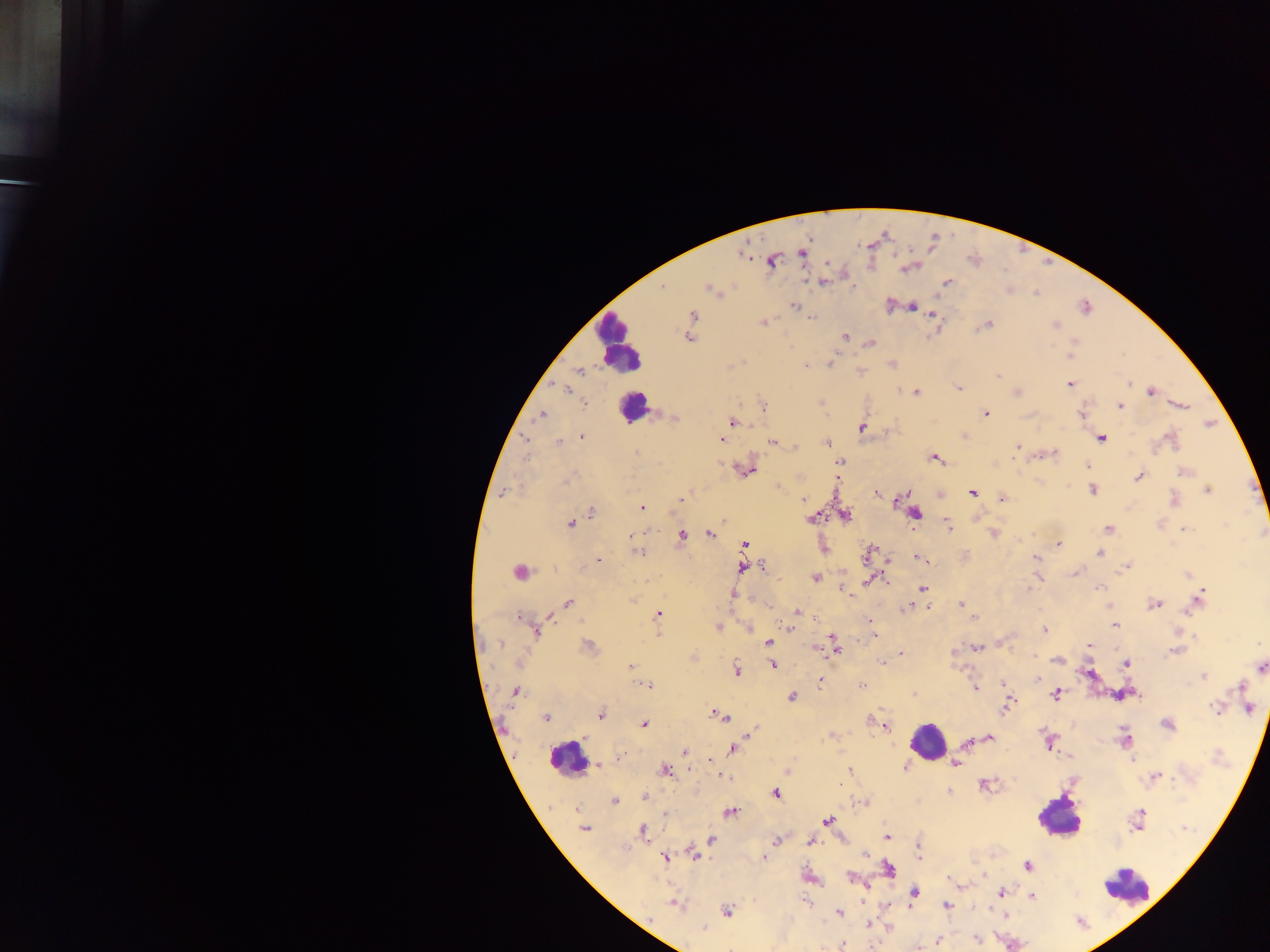

Approximate centers as {x, y} in pixels.
Summary:
  - Leukocyte locations: {618, 343}, {633, 406}, {927, 740}, {567, 758}, {1058, 816}, {1126, 886}
  - Malaria parasite locations: {742, 252}, {802, 253}, {773, 260}, {827, 263}, {907, 267}, {823, 282}, {947, 283}, {662, 286}, {710, 288}, {890, 305}, {794, 306}, {911, 306}, {933, 314}, {691, 316}, {812, 317}, {763, 322}, {987, 324}, {1056, 324}, {845, 336}, {690, 337}, {1073, 340}, {871, 343}, {1070, 355}, {830, 362}, {892, 364}, {805, 366}, {578, 369}, {861, 370}, {997, 375}, {1070, 384}, {566, 388}, {959, 388}, {1016, 391}, {1149, 391}, {914, 392}, {584, 402}, {821, 402}, {1180, 404}, {762, 405}, {1120, 406}, {986, 413}, {540, 414}, {1081, 414}, {672, 416}, {732, 421}, {1209, 423}, {862, 427}, {965, 435}, {582, 437}, {523, 438}, {720, 438}, {1100, 438}, {1171, 440}, {772, 441}, {558, 442}, {825, 443}, {1017, 446}, {795, 447}, {1052, 453}, {636, 454}, {934, 458}, {839, 463}, {1087, 465}, {744, 469}, {1184, 471}, {799, 476}, {1139, 476}, {777, 485}, {1092, 490}, {1207, 490}, {503, 492}, {972, 492}, {877, 493}, {903, 495}, {941, 495}, {1003, 498}, {681, 499}, {803, 499}, {1174, 500}, {642, 507}, {591, 512}, {915, 514}, {844, 515}, {811, 517}, {975, 517}, {724, 520}, {570, 523}, {947, 524}, {1108, 529}, {1184, 529}, {709, 533}, {993, 533}, {629, 535}, {681, 536}, {1057, 543}, {744, 545}, {823, 547}, {638, 552}, {868, 553}, {1099, 553}, {920, 558}, {886, 559}, {1035, 559}, {598, 561}, {762, 566}, {1126, 566}, {743, 567}, {519, 572}, {1075, 573}, {1187, 575}, {1038, 576}, {814, 577}, {869, 579}, {923, 588}, {842, 590}, {1027, 590}, {733, 593}, {1198, 599}, {568, 603}, {1154, 603}, {961, 604}, {927, 606}, {1109, 606}, {907, 607}, {797, 612}, {657, 614}, {518, 617}, {974, 617}, {870, 622}, {1112, 623}, {1115, 624}, {718, 627}, {749, 628}, {789, 628}, {1043, 629}, {535, 631}, {657, 632}, {1178, 632}, {874, 636}, {833, 639}, {768, 642}, {998, 643}, {588, 646}, {1089, 646}, {833, 647}, {813, 648}, {976, 648}, {1175, 651}, {901, 653}, {952, 654}, {694, 657}, {1056, 659}, {882, 662}, {1126, 663}, {771, 664}, {631, 667}, {1260, 667}, {736, 670}, {1088, 672}, {1203, 676}, {1037, 678}, {819, 680}, {1003, 683}, {648, 685}, {861, 685}, {1240, 686}, {975, 688}, {515, 691}, {1123, 693}, {915, 694}, {1056, 695}, {791, 697}, {1007, 704}, {1217, 707}, {1249, 708}, {600, 714}, {718, 715}, {546, 717}, {869, 720}, {1167, 724}, {643, 725}, {885, 725}, {753, 731}, {831, 735}, {989, 738}, {1125, 739}, {969, 742}, {1048, 742}, {733, 748}, {685, 751}, {621, 753}, {1068, 757}, {1132, 758}, {710, 759}, {956, 763}, {598, 764}, {905, 767}, {665, 770}, {787, 770}, {850, 770}, {722, 775}, {1154, 777}, {983, 784}, {948, 791}, {775, 793}, {645, 797}, {614, 801}, {864, 802}, {665, 812}, {729, 812}, {1137, 819}, {827, 821}, {584, 828}, {642, 831}, {886, 836}, {711, 839}, {775, 840}, {810, 841}, {918, 845}, {865, 854}, {693, 855}, {919, 855}, {665, 856}, {764, 858}, {1027, 866}, {887, 869}, {984, 875}, {809, 877}, {850, 878}, {961, 885}, {914, 891}, {1002, 891}, {1030, 896}, {675, 904}, {909, 906}, {947, 906}, {727, 911}, {839, 913}, {1004, 916}, {867, 924}, {888, 926}, {704, 927}, {976, 939}, {937, 941}, {842, 944}
  - Country: Ghana
  - Field of view: single
  - Capture: mobile-phone photograph through a microscope
  - Image size: 1270×952 pixels
  - Preparation: thick blood film